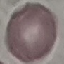
Summary:
  - Malaria status: uninfected
  - Capture: smartphone through the microscope eyepiece
  - Image type: automatically extracted cell patch, resized to 64 × 64 pixels
  - Stain: Giemsa
  - Preparation: thin smear